Locate every Plasmodium parasite.
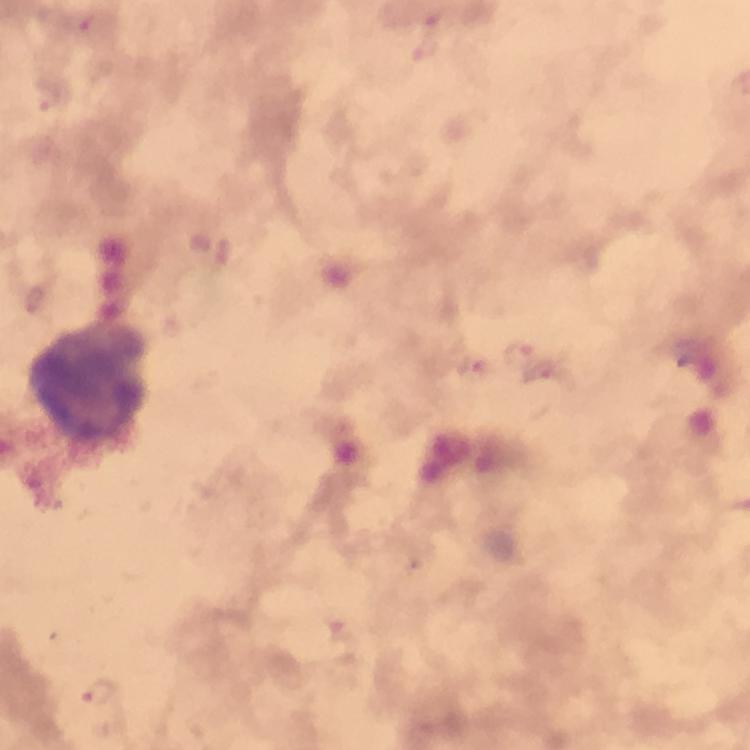

Approximate centers as (x, y) in pixels.
Plasmodium parasites: (426, 50), (51, 95), (224, 255), (519, 352), (473, 369), (545, 375), (100, 693).

image size = 750×750 pixels
magnification = 100x
leukocyte locations = approximate centers as (x, y) in pixels: (87, 380)
stain = Giemsa
context = from a diagnostic examination for malaria
immersion oil = used
preparation = thick blood film
capture = smartphone mounted on the microscope
cropped from = a single field of view